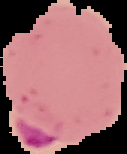 Image is 127×154 pixels. The area outside the segmented cell region is set to black. From a thin blood film. Malaria status: parasitized.